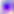

Summary:
  - Modality: photomicrograph
  - Magnification: 400x
  - Identification: Toxoplasma gondii